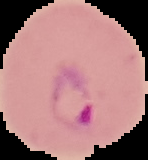
Summary:
  - Image type: segmented cell region on a black background
  - Image size: 148×160 pixels
  - Preparation: thin blood smear
  - Result: Plasmodium parasites detected